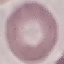

Summary:
  - Result: negative for malaria parasites
  - Preparation: thin smear
  - Capture: smartphone through the microscope eyepiece
  - Stain: Giemsa
  - Image type: automatically extracted cell patch, resized to 64 × 64 pixels